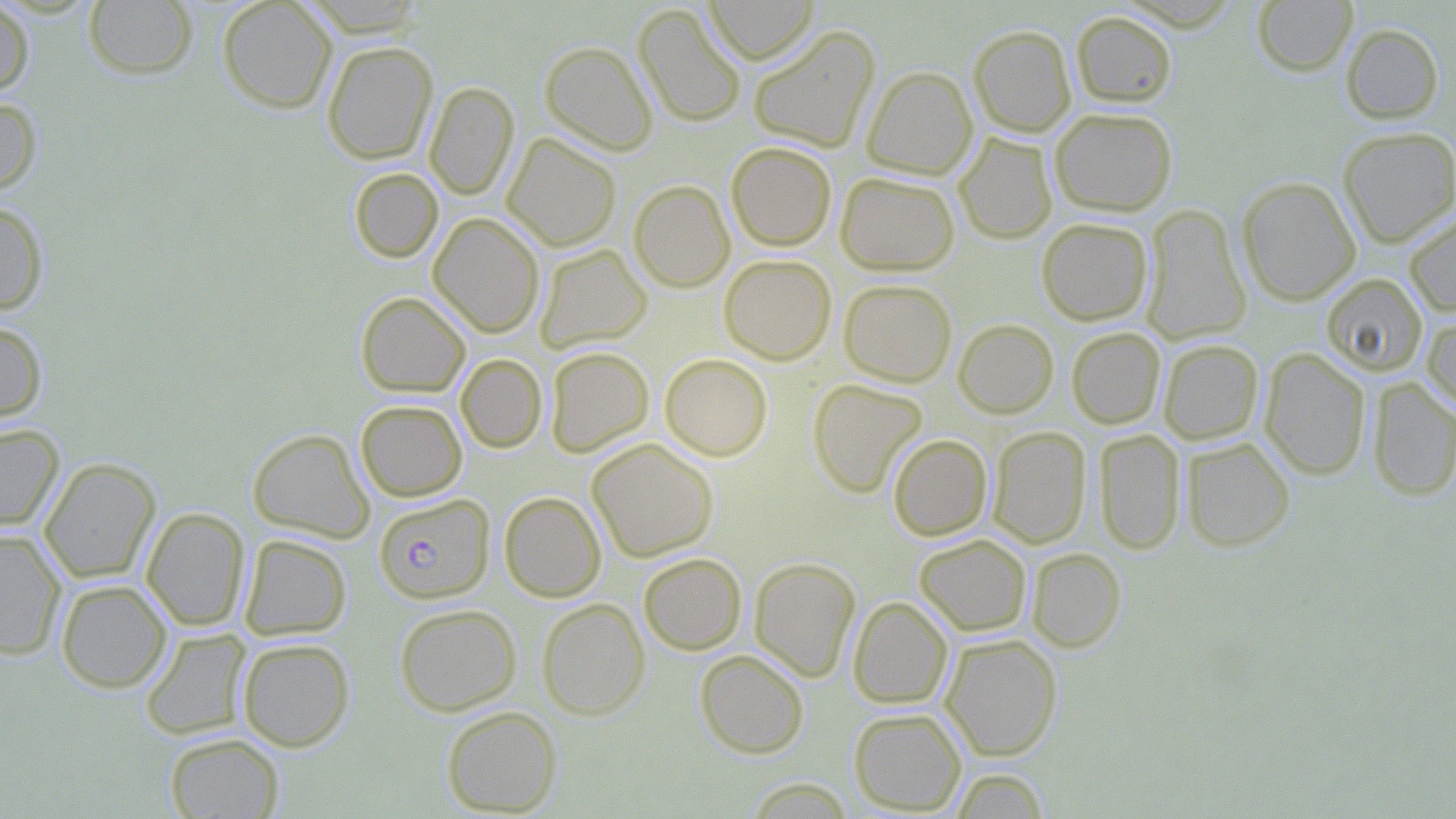 Approximate bounding boxes as (x1, y1, x2, y2) in pixels. Plasmodium falciparum-infected red blood cell locations: (377, 495, 497, 605). Uninfected red blood cell locations: (0, 0, 34, 99), (217, 0, 338, 113), (704, 0, 818, 64), (1253, 0, 1358, 76), (83, 1, 198, 79), (634, 4, 746, 128), (1071, 11, 1177, 108), (969, 24, 1076, 137), (1340, 24, 1444, 124), (747, 25, 881, 153), (322, 40, 438, 165), (540, 41, 658, 156), (862, 66, 978, 180), (424, 81, 519, 200), (0, 96, 43, 197), (1049, 107, 1178, 216), (1338, 127, 1456, 247), (502, 133, 621, 251), (954, 133, 1057, 244), (726, 142, 837, 251), (349, 167, 443, 263), (835, 171, 960, 275), (1236, 176, 1361, 306), (628, 179, 735, 292), (0, 199, 49, 315), (1142, 204, 1252, 345), (1404, 211, 1456, 317), (428, 213, 545, 338), (1036, 217, 1153, 326), (535, 244, 652, 352), (719, 254, 836, 364), (1321, 272, 1428, 376), (838, 278, 957, 387), (356, 291, 470, 397), (1421, 308, 1456, 416), (953, 318, 1059, 418), (0, 320, 49, 424), (1066, 327, 1166, 429), (1158, 339, 1264, 445), (545, 346, 654, 456), (1259, 348, 1371, 480), (455, 353, 547, 453), (660, 353, 773, 461), (1368, 377, 1456, 501), (808, 378, 928, 498), (355, 399, 467, 501), (0, 423, 64, 532), (987, 426, 1091, 548), (248, 428, 374, 543), (1094, 428, 1186, 555), (887, 433, 993, 541), (1181, 437, 1295, 551), (587, 438, 719, 562), (39, 457, 161, 583), (499, 491, 606, 602), (141, 507, 250, 631), (0, 530, 67, 661), (239, 534, 352, 640), (914, 534, 1032, 636), (1027, 548, 1126, 652), (638, 552, 747, 655), (749, 557, 861, 682), (55, 579, 172, 693), (848, 596, 953, 709), (537, 598, 649, 721), (394, 603, 522, 715), (140, 628, 251, 740), (941, 634, 1062, 761), (236, 637, 355, 752), (695, 649, 809, 758), (441, 705, 562, 816), (848, 707, 967, 815), (164, 732, 285, 818), (948, 767, 1050, 818), (744, 777, 855, 818). Slide-level diagnosis: Plasmodium falciparum. Optical microscopy. Image is 1456×819 pixels. Single field of view. May-Grünwald-Giemsa-stained preparation. 1000x magnification. Thin blood smear.